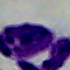

Micrograph. 1000x magnification. A leukocyte is seen.